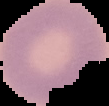
Summary:
  - Image type: segmented cell region on a black background
  - Image size: 109×106 pixels
  - Preparation: thin blood smear
  - Result: no Plasmodium parasites detected